Classify this cell by malaria status.
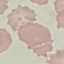
It is uninfected.

Giemsa-stained preparation. Thin blood film. Photographed with a smartphone camera at the microscope eyepiece. Cell patch, automatically extracted from a larger field of view and resized to 64 × 64 pixels.